Locate and identify every blood parasite.
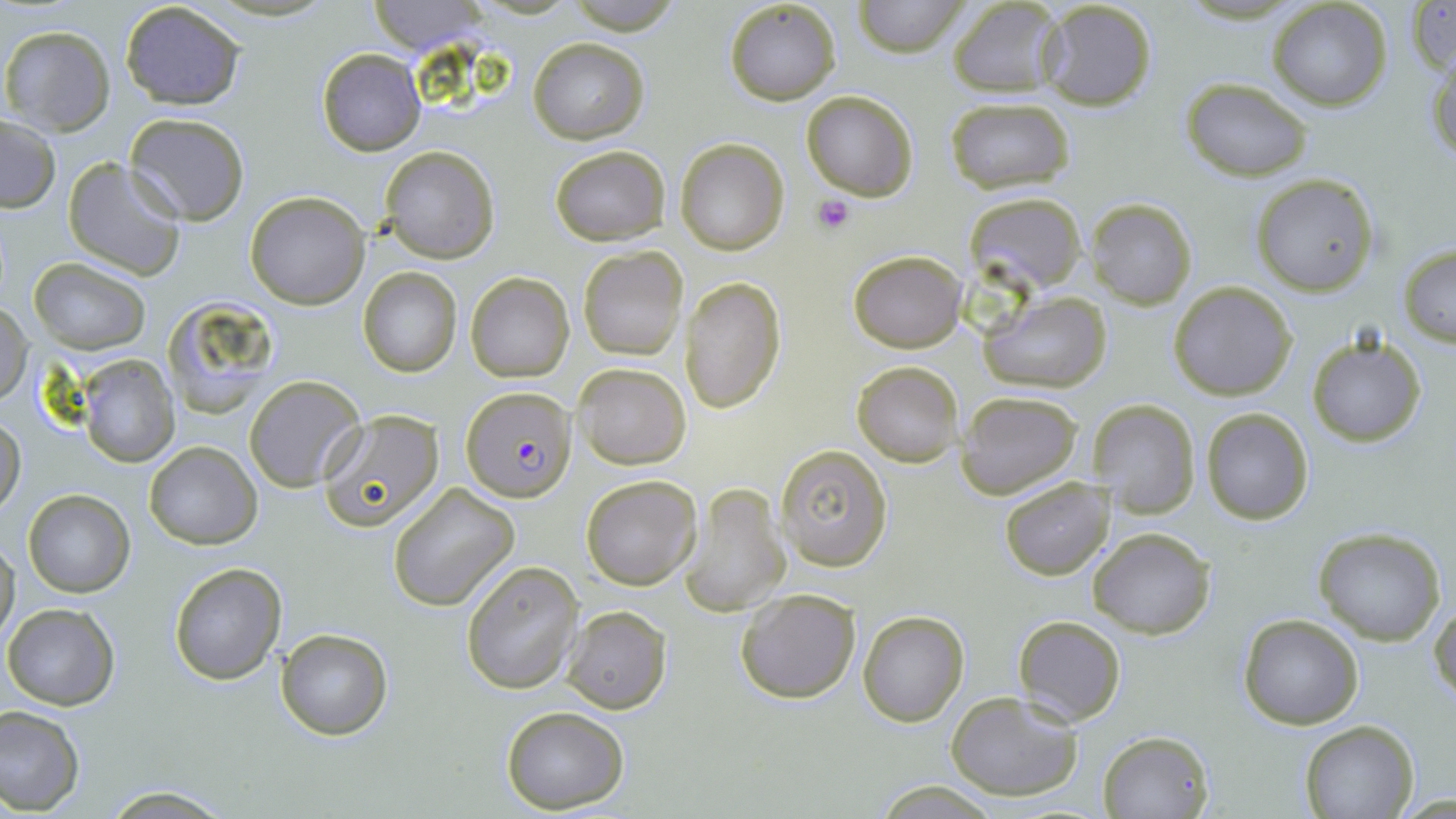

Approximate bounding boxes as (x1, y1, x2, y2) in pixels.
Plasmodium falciparum-infected red blood cells: (461, 387, 576, 504).
No Plasmodium ovale, Plasmodium malariae, Plasmodium vivax, Babesia divergens, or Trypanosoma brucei observed.

slide-level diagnosis = Plasmodium falciparum
magnification = 1000x
image size = 1456×819 pixels
stain = May-Grünwald-Giemsa
modality = light microscopy
preparation = thin blood film
platelet locations = approximate bounding boxes as (x1, y1, x2, y2) in pixels: (812, 192, 856, 234)
uninfected red blood cell locations = approximate bounding boxes as (x1, y1, x2, y2) in pixels: (855, 0, 965, 56), (363, 1, 488, 52), (724, 1, 842, 105), (946, 1, 1064, 96), (1039, 1, 1159, 113), (1408, 1, 1455, 75), (119, 2, 247, 110), (1268, 2, 1392, 110), (2, 25, 116, 135), (527, 36, 649, 145), (317, 48, 425, 156), (1427, 48, 1456, 166), (1181, 78, 1313, 182), (802, 91, 918, 200), (944, 96, 1076, 194), (124, 112, 251, 225), (1, 116, 61, 212), (676, 137, 789, 255), (549, 144, 670, 245), (379, 145, 500, 263), (62, 156, 186, 281), (1251, 173, 1380, 297), (245, 191, 370, 310), (968, 193, 1085, 291), (1088, 199, 1196, 309), (1398, 244, 1456, 346), (577, 245, 688, 361), (848, 250, 967, 352), (29, 257, 150, 355), (357, 268, 462, 377), (466, 272, 573, 383), (681, 277, 786, 415), (1169, 281, 1297, 401), (980, 291, 1113, 393), (162, 298, 283, 418), (1, 303, 32, 407), (1306, 333, 1427, 449), (75, 354, 180, 466), (852, 360, 964, 466), (573, 363, 691, 470), (244, 374, 365, 493), (956, 391, 1085, 500), (1087, 399, 1200, 520), (1200, 408, 1314, 525), (319, 410, 443, 531), (0, 415, 26, 515), (145, 441, 262, 549), (774, 444, 891, 572), (581, 474, 702, 591), (999, 475, 1115, 581), (388, 481, 520, 610), (681, 483, 791, 616), (23, 490, 135, 598), (1088, 528, 1216, 638), (1312, 528, 1447, 645), (0, 536, 19, 646), (460, 560, 583, 694), (168, 563, 287, 684), (735, 587, 861, 706), (1429, 601, 1456, 709), (3, 604, 120, 711), (563, 605, 673, 715), (857, 609, 970, 726), (1237, 612, 1365, 731), (1012, 615, 1126, 726), (276, 628, 393, 741), (946, 690, 1086, 802), (0, 705, 85, 815), (500, 706, 630, 812), (1299, 719, 1420, 818), (1098, 729, 1213, 818), (873, 781, 1000, 816), (99, 787, 236, 817)
field of view = one of a larger specimen